Comment on the morphology of the erythrocytes.
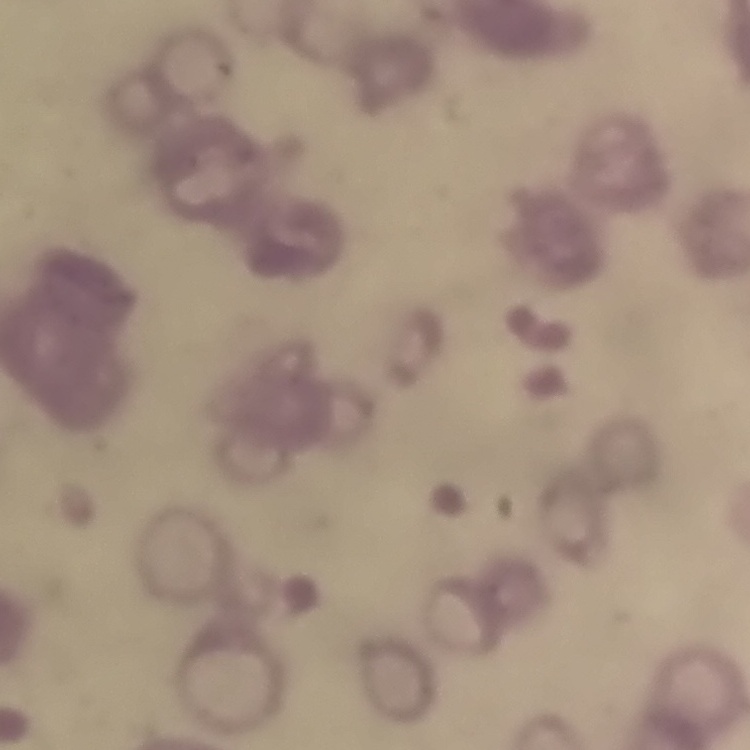

They show rouleaux formation.

Thin blood smear. Square crop of a larger photomicrograph. Field's or Giemsa stain.